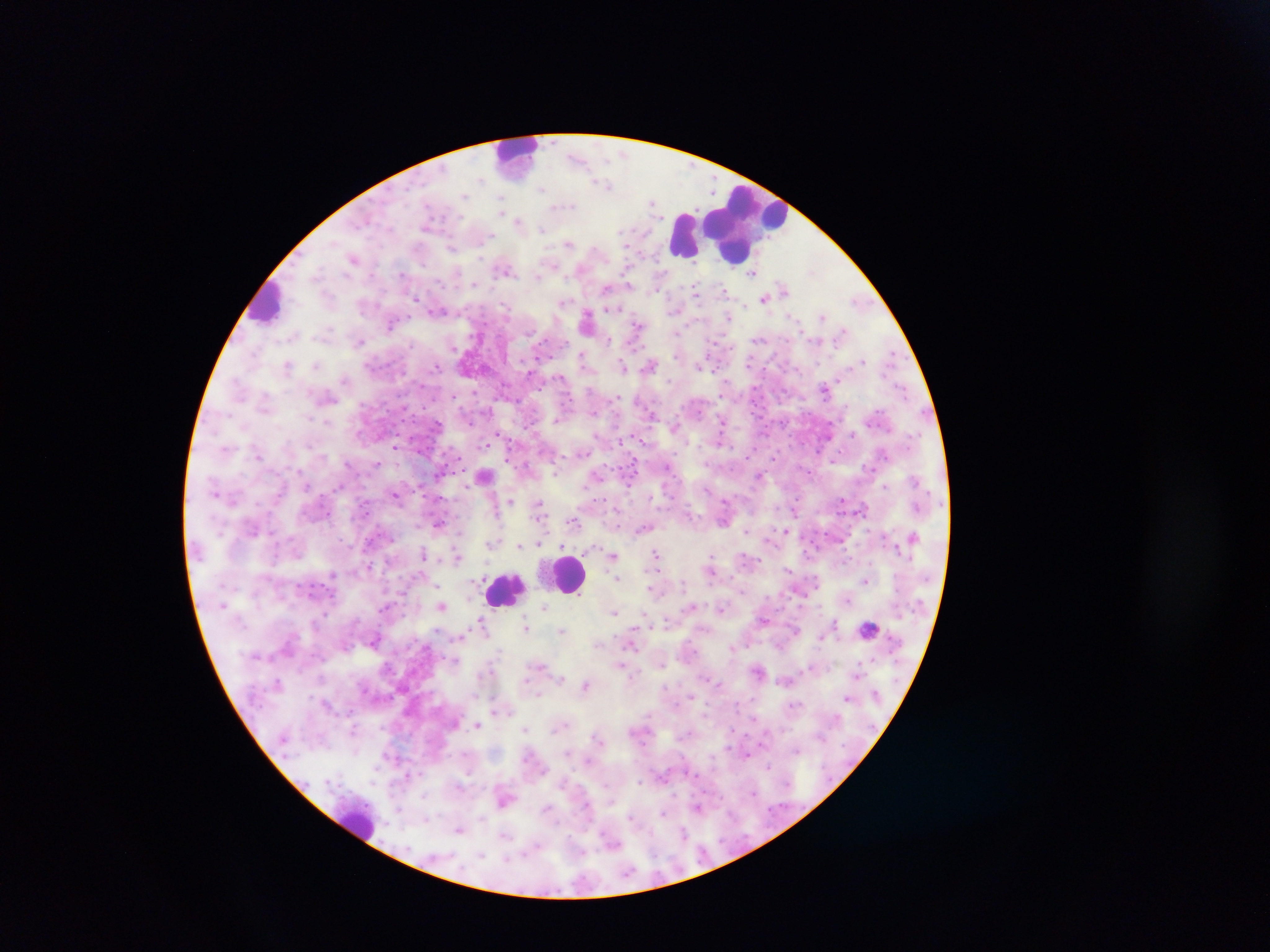
image size = 1270×952 pixels
Plasmodium parasite locations = approximate centers as x y in pixels: 577 157; 607 185; 653 202; 520 222; 541 228; 569 244; 453 247; 354 257; 504 267; 752 273; 608 288; 697 289; 784 289; 769 294; 765 297; 859 300; 563 302; 437 310; 729 316; 822 317; 587 322; 392 323; 638 324; 843 332; 678 333; 608 339; 361 341; 891 354; 584 360; 861 362; 288 365; 650 365; 315 366; 624 366; 700 366; 345 380; 825 388; 557 419; 529 425; 675 427; 498 434; 643 440; 395 446; 258 455; 376 464; 668 466; 596 475; 759 475; 485 476; 884 488; 395 493; 842 499; 511 501; 539 504; 917 506; 863 508; 795 510; 574 521; 439 524; 643 527; 746 530; 787 531; 913 536; 769 539; 491 542; 538 543; 519 545; 656 554; 423 555; 613 555; 458 556; 369 567; 710 569; 789 569; 865 581; 652 588; 847 599; 691 606; 442 607; 544 608; 721 608; 614 613; 482 620; 764 620; 833 623; 526 627; 562 630; 796 630; 822 638; 632 639; 599 645; 733 646; 780 646; 620 663; 758 671; 858 675; 561 678; 586 684; 692 696; 847 698; 497 709; 479 726; 354 729; 526 729; 598 739; 568 753; 747 755; 768 767; 409 775; 459 787; 505 799; 699 807; 548 808; 664 812; 425 818; 459 829; 685 833; 505 834
preparation = thick blood film
field of view = single
leukocyte locations = approximate centers as x y in pixels: 517 154; 743 224; 684 236; 268 302; 569 573; 507 590; 869 627; 358 823
country = Ghana
capture = mobile-phone photograph through a microscope